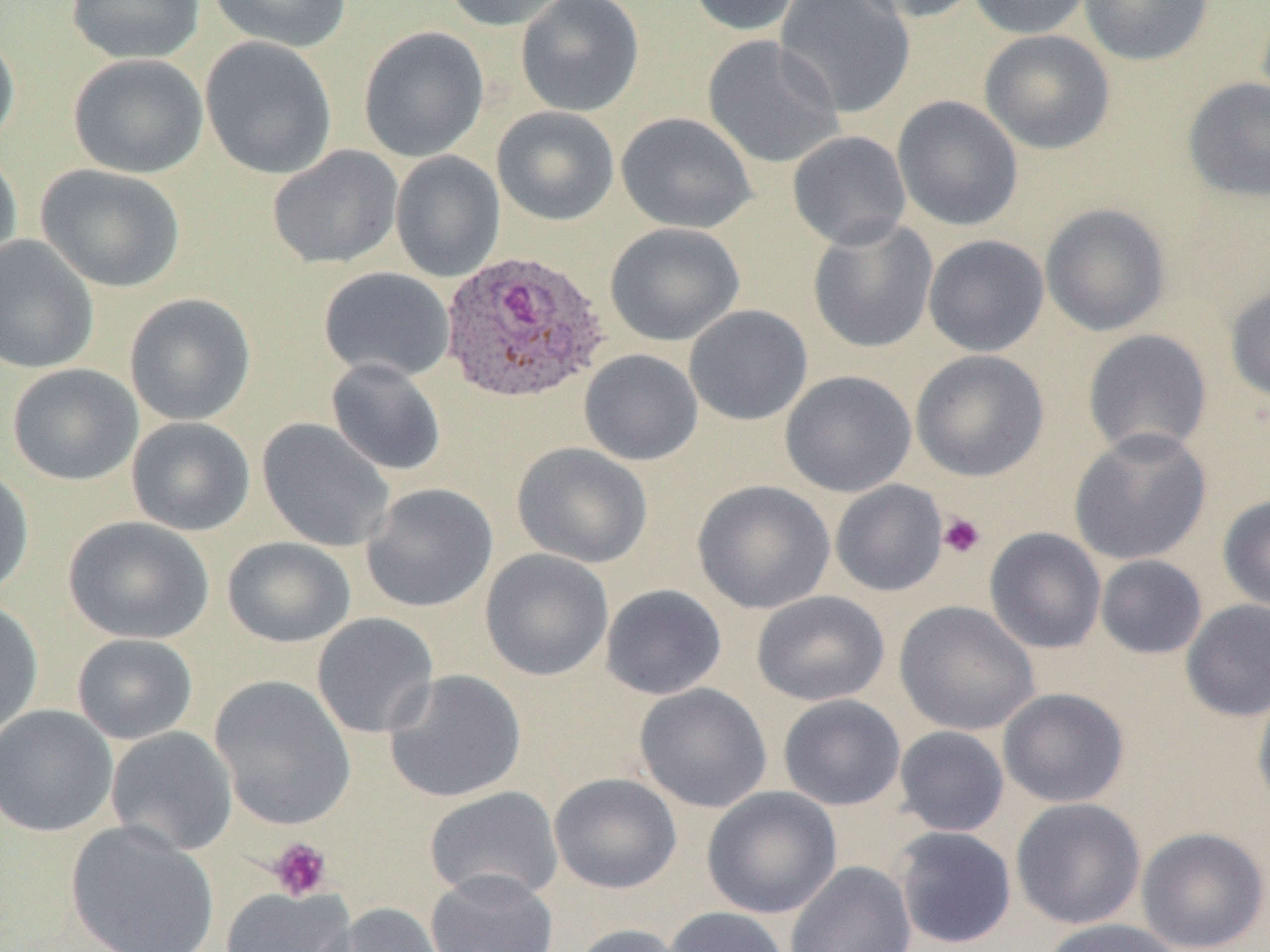
Summary:
  - Coordinate format: approximate bounding boxes as (x1, y1, x2, y2) in pixels
  - Plasmodium ovale-infected red blood cell locations: (439, 248, 611, 404)
  - Platelet locations: (937, 513, 986, 559), (268, 837, 332, 901)
  - Uninfected red blood cell locations: (66, 0, 205, 64), (207, 0, 353, 53), (442, 0, 575, 32), (515, 0, 645, 117), (687, 0, 804, 36), (775, 0, 915, 118), (850, 0, 984, 23), (968, 0, 1094, 39), (1078, 0, 1214, 66), (358, 26, 490, 162), (0, 27, 20, 153), (980, 29, 1115, 154), (703, 35, 844, 169), (200, 36, 338, 180), (68, 53, 209, 178), (1182, 77, 1270, 203), (892, 95, 1023, 231), (492, 106, 619, 226), (615, 111, 758, 234), (787, 130, 911, 250), (267, 145, 403, 270), (0, 148, 22, 273), (389, 151, 506, 283), (36, 164, 186, 293), (1040, 203, 1172, 337), (808, 218, 938, 354), (605, 222, 745, 346), (0, 235, 99, 375), (923, 235, 1049, 357), (318, 266, 455, 382), (1225, 282, 1270, 404), (124, 293, 256, 426), (684, 304, 813, 426), (1082, 329, 1213, 458), (578, 349, 703, 465), (911, 349, 1049, 482), (325, 358, 447, 476), (6, 363, 143, 486), (780, 370, 916, 497), (126, 416, 255, 537), (256, 418, 396, 552), (1069, 427, 1212, 565), (512, 442, 652, 569), (0, 467, 34, 599), (830, 479, 947, 597), (693, 480, 836, 614), (361, 483, 498, 613), (1218, 494, 1270, 614), (63, 516, 214, 644), (984, 527, 1107, 654), (222, 536, 357, 648), (479, 549, 614, 681), (1095, 555, 1208, 660), (599, 584, 727, 700), (752, 590, 889, 706), (0, 598, 44, 738), (1180, 599, 1270, 722), (894, 601, 1040, 736), (312, 613, 439, 739), (72, 633, 198, 745), (384, 668, 526, 804), (209, 674, 357, 830), (635, 683, 772, 813), (1252, 683, 1270, 817), (997, 687, 1129, 808), (778, 694, 906, 811), (0, 705, 118, 838), (893, 725, 1010, 837), (105, 726, 238, 857), (548, 772, 682, 894), (424, 786, 564, 904), (702, 786, 842, 919), (1010, 798, 1146, 930), (65, 821, 220, 952), (892, 826, 1017, 949), (1136, 826, 1270, 952), (785, 861, 917, 952), (425, 869, 558, 952), (220, 886, 356, 952), (320, 903, 450, 952), (663, 906, 789, 952), (1037, 918, 1184, 952), (568, 924, 686, 952)
  - Slide-level diagnosis: Plasmodium ovale
  - Preparation: thin blood film
  - Image size: 1270×952 pixels
  - Modality: optical microscopy
  - Field of view: single
  - Magnification: 1000x